Give the extent of all uninfected red blood cells.
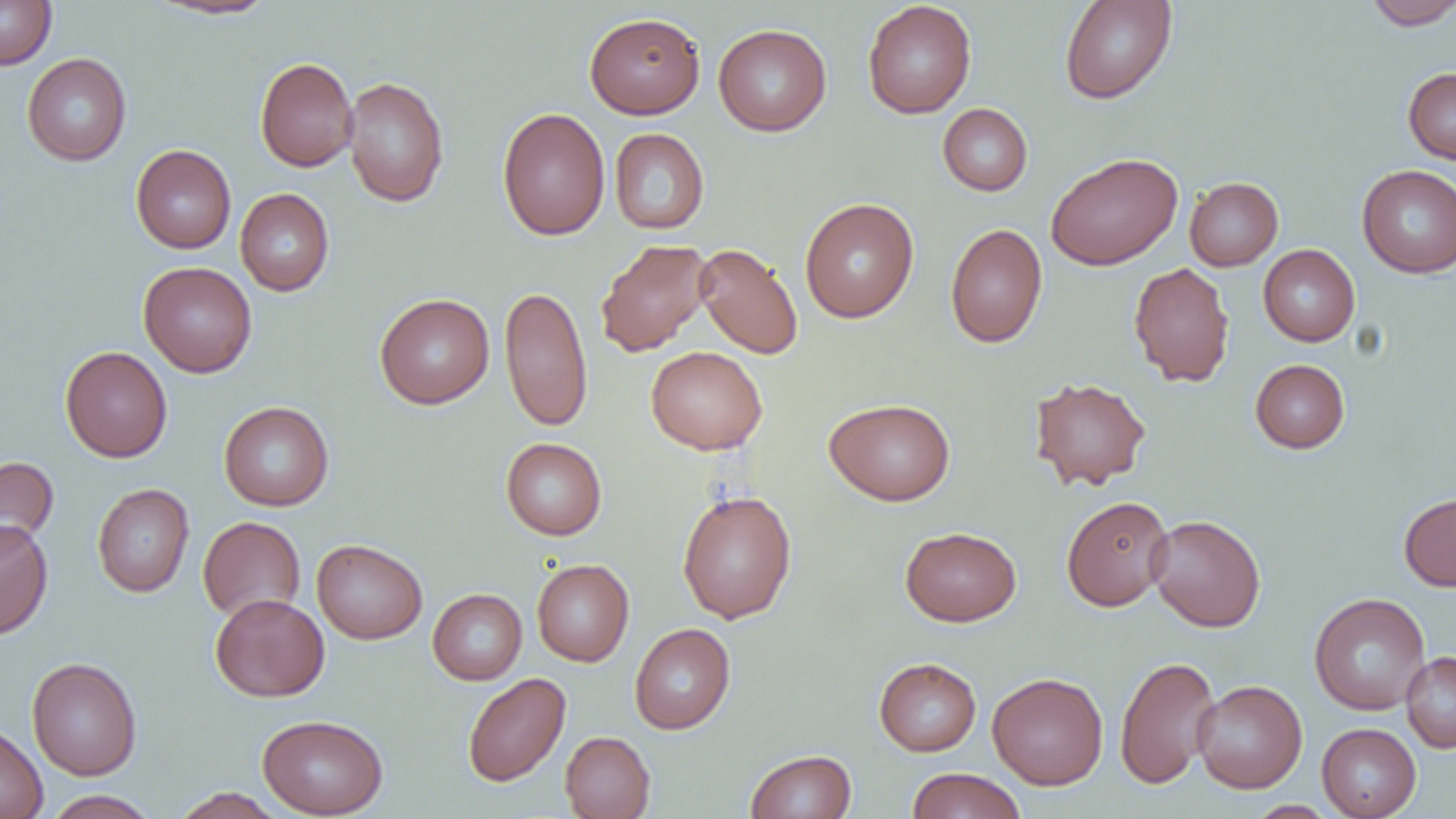
Approximate bounding boxes as (x1, y1, x2, y2) in pixels.
Uninfected red blood cells: (0, 0, 57, 69), (1059, 0, 1177, 105), (148, 1, 280, 20), (862, 1, 977, 118), (1363, 1, 1456, 30), (584, 12, 705, 118), (713, 23, 832, 136), (22, 53, 132, 166), (255, 56, 358, 172), (1403, 67, 1456, 166), (342, 76, 449, 207), (937, 103, 1033, 196), (497, 107, 611, 241), (609, 128, 709, 234), (131, 144, 236, 253), (1045, 152, 1182, 270), (1357, 165, 1456, 278), (1184, 177, 1283, 271), (235, 188, 335, 296), (799, 197, 919, 323), (945, 223, 1047, 348), (595, 239, 713, 357), (694, 244, 803, 359), (1258, 244, 1360, 346), (138, 261, 257, 377), (1128, 262, 1235, 387), (499, 285, 594, 431), (375, 293, 494, 409), (59, 346, 173, 462), (645, 346, 767, 454), (1250, 359, 1350, 453), (1029, 377, 1152, 491), (824, 398, 955, 505), (219, 401, 335, 511), (501, 437, 607, 540), (0, 455, 59, 558), (92, 483, 194, 598), (677, 490, 797, 623), (1398, 492, 1456, 591), (1061, 495, 1174, 611), (1147, 514, 1266, 632), (198, 516, 305, 621), (0, 519, 53, 640), (900, 526, 1021, 626), (312, 538, 427, 644), (531, 559, 634, 666), (427, 588, 527, 685), (1309, 592, 1431, 715), (210, 593, 329, 702), (629, 623, 735, 734), (1401, 652, 1456, 753), (1114, 655, 1220, 789), (26, 657, 142, 780), (874, 657, 981, 756), (462, 672, 571, 787), (987, 672, 1108, 790), (1192, 679, 1307, 793), (257, 714, 389, 818), (0, 721, 48, 819), (1317, 723, 1421, 819), (559, 731, 655, 819), (745, 749, 857, 818), (906, 767, 1026, 819), (171, 787, 286, 819), (43, 790, 161, 819), (1245, 801, 1339, 818).

Summary:
  - Slide-level diagnosis: negative for blood parasites
  - Preparation: thin blood film
  - Field of view: single
  - Modality: light microscopy
  - Magnification: 1000x
  - Image size: 1456×819 pixels